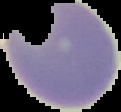
Summary:
  - Result: negative for Plasmodium parasites
  - Preparation: thin blood smear
  - Image type: segmented cell region with the area outside set to black
  - Image size: 121×112 pixels